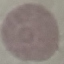
{
  "malaria_status": "uninfected",
  "image_type": "automatically extracted cell patch, resized to 64 × 64 pixels",
  "stain": "Giemsa",
  "preparation": "thin blood film",
  "capture": "smartphone camera at the microscope eyepiece"
}